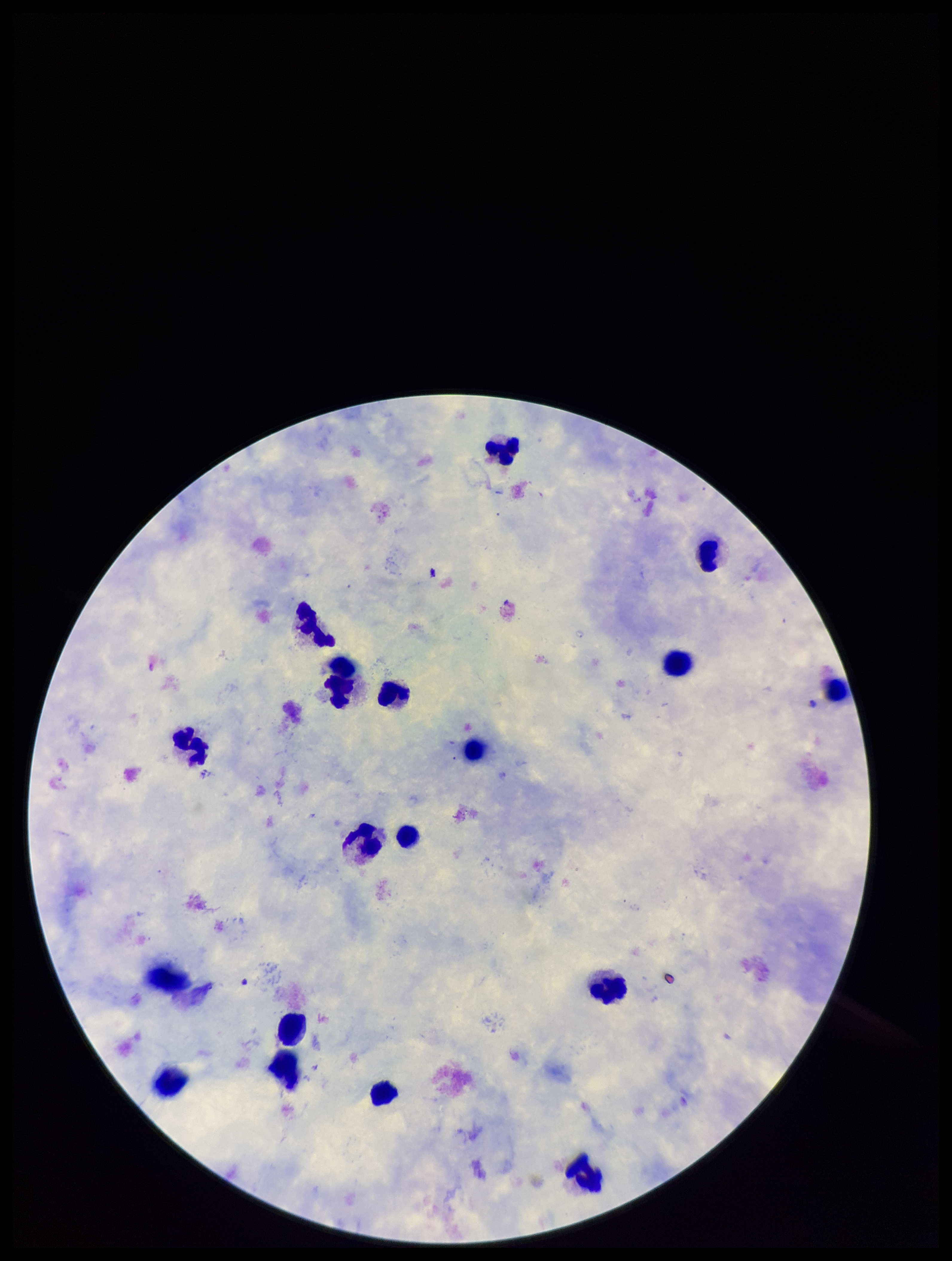

Summary:
  - Plasmodium parasites: seen
  - Species reported for this patient: Plasmodium falciparum
  - Field of view: single
  - Patient malaria status: positive
  - Capture: smartphone photograph through the microscope eyepiece
  - Image size: 952×1261 pixels
  - Leukocyte count: 18
  - Preparation: thick
  - Parasite count: 1
  - Stain: Giemsa